Locate every blood parasite and identify its species.
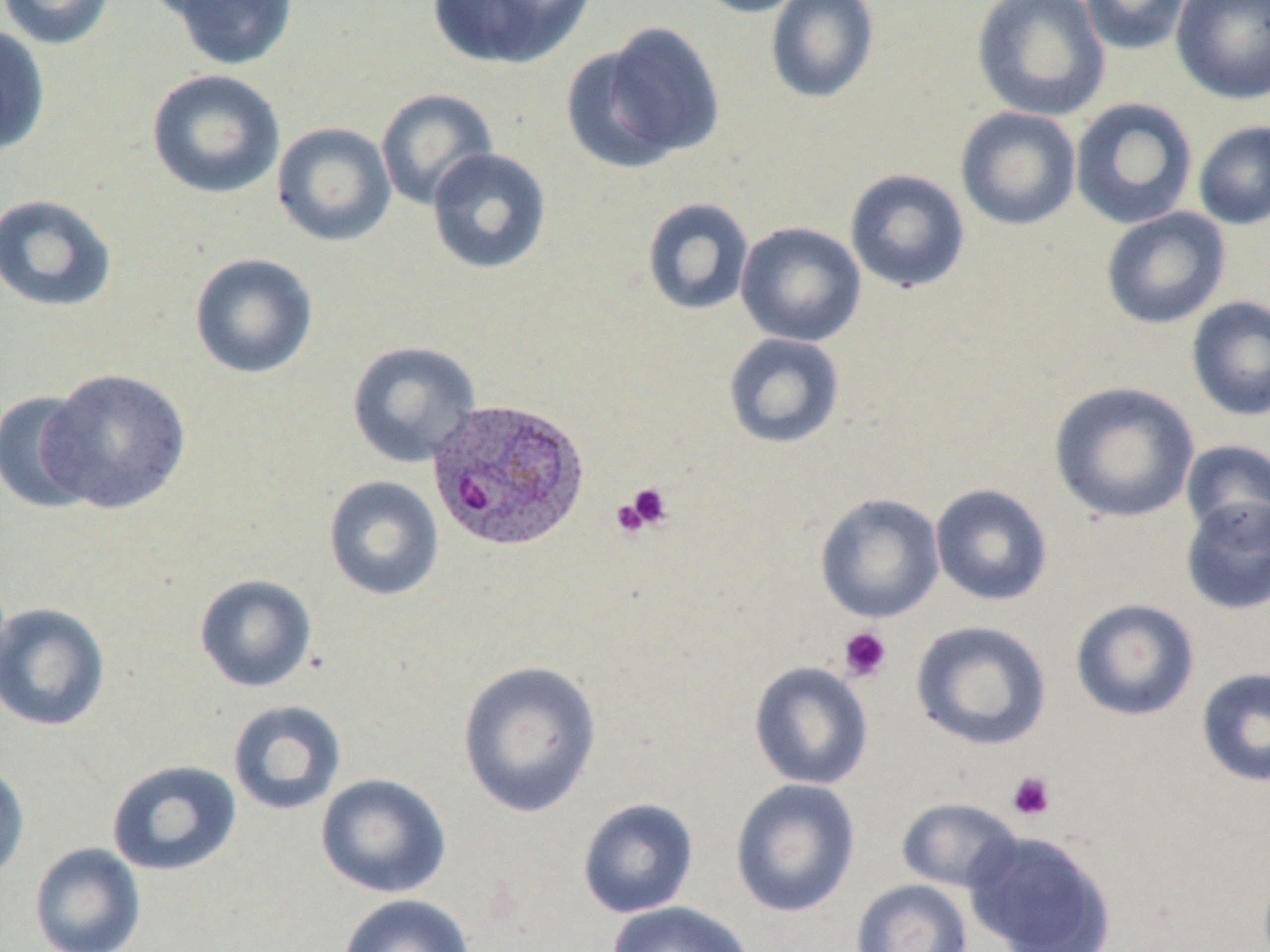
Approximate bounding boxes as (x1,y1)-(x2,y2) corner pairs in pixels.
Plasmodium ovale-infected red blood cells: (426,397)-(591,553).
No Plasmodium falciparum, Plasmodium malariae, Plasmodium vivax, Babesia divergens, or Trypanosoma brucei observed.

Platelet locations: (620,482)-(673,534), (838,626)-(892,683), (1007,771)-(1056,822). Uninfected red blood cell locations: (0,0)-(116,50), (161,0)-(300,71), (426,0)-(594,69), (691,0)-(813,18), (765,0)-(880,104), (971,0)-(1111,122), (1080,0)-(1193,55), (1171,0)-(1270,104), (566,21)-(725,173), (0,23)-(51,156), (145,69)-(286,200), (376,88)-(498,210), (1069,97)-(1198,230), (955,107)-(1082,231), (1193,120)-(1270,230), (272,122)-(397,247), (426,147)-(552,274), (845,168)-(970,293), (0,193)-(118,314), (642,197)-(755,316), (1100,207)-(1231,330), (735,221)-(867,348), (189,252)-(319,379), (1186,296)-(1270,422), (723,332)-(845,449), (347,340)-(481,468), (38,367)-(192,515), (1048,381)-(1200,524), (0,389)-(101,514), (1179,440)-(1270,541), (323,475)-(444,601), (930,483)-(1053,606), (815,492)-(945,624), (1179,495)-(1270,616), (194,574)-(317,693), (1070,598)-(1200,721), (0,602)-(110,732), (911,620)-(1052,751), (456,660)-(602,818), (749,661)-(873,790), (1196,666)-(1270,788), (227,700)-(347,816), (0,757)-(30,885), (106,759)-(242,877), (315,773)-(451,899), (730,778)-(860,918), (577,797)-(699,919), (896,797)-(1022,893), (966,831)-(1116,952), (29,842)-(146,952), (850,879)-(974,952), (337,894)-(476,952), (606,900)-(756,952). Slide-level diagnosis: Plasmodium ovale. May-Grünwald-Giemsa-stained preparation. Captured at 1000x magnification. Light microscopy. Thin blood film. Single field of view. Image is 1270×952 pixels.